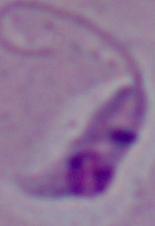
Summary:
  - Modality: photomicrograph
  - Magnification: 1000x
  - Identification: Leishmania